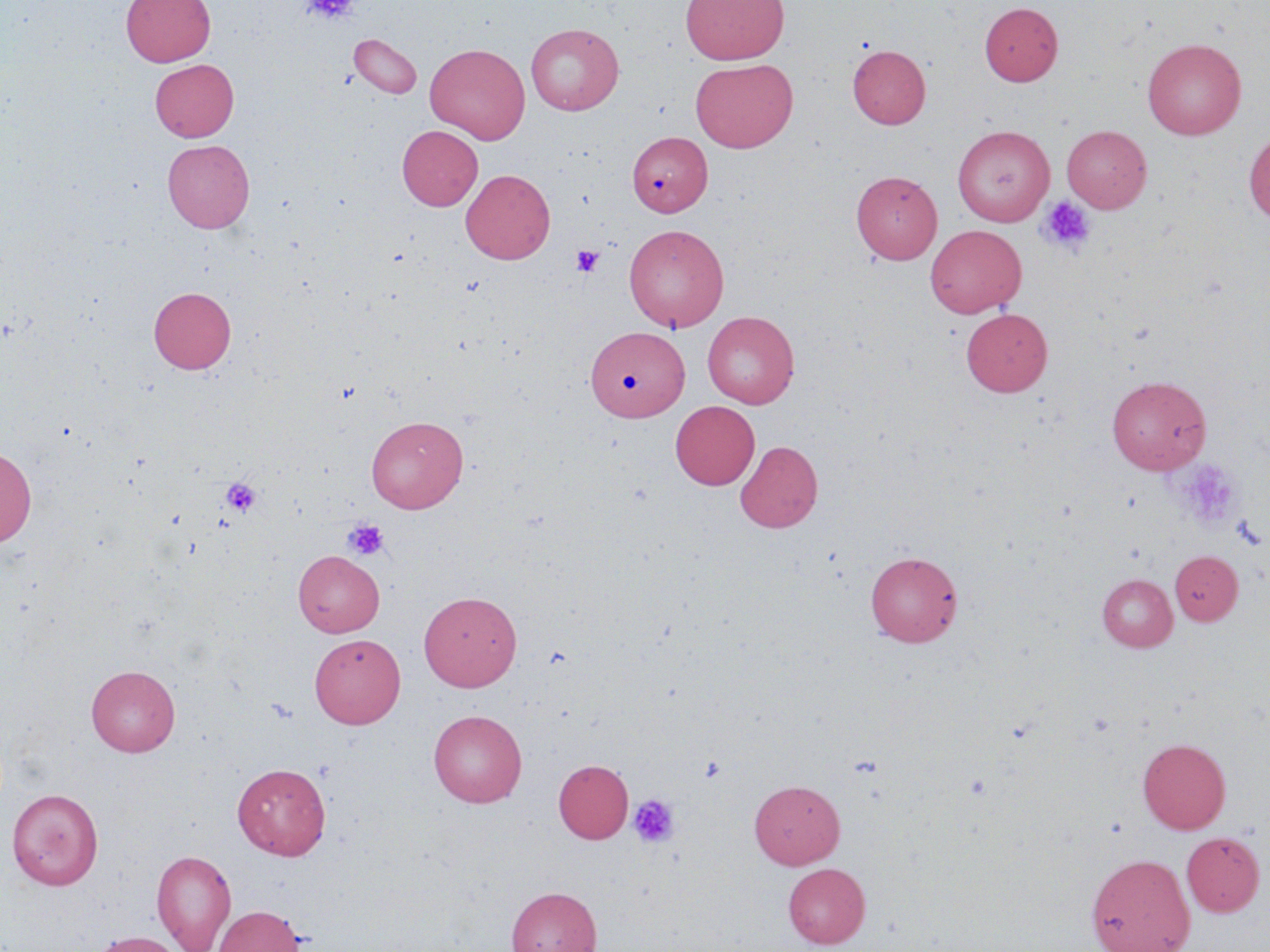
Summary:
  - Coordinate format: approximate bounding boxes as (x1, y1, x2, y2) in pixels
  - Platelet locations (subset): (302, 0, 360, 23), (1036, 195, 1096, 256), (571, 244, 604, 277), (1176, 459, 1242, 529), (221, 478, 261, 518), (342, 518, 389, 561), (699, 755, 726, 783), (628, 794, 680, 848)
  - Uninfected red blood cell locations (subset): (121, 0, 216, 66), (680, 0, 789, 64), (979, 2, 1062, 85), (525, 22, 624, 116), (349, 33, 422, 99), (1142, 38, 1246, 140), (425, 43, 530, 144), (848, 45, 931, 128), (150, 58, 239, 142), (690, 59, 798, 152), (397, 125, 482, 211), (953, 125, 1055, 226), (1244, 130, 1270, 224), (627, 132, 712, 217), (163, 139, 254, 233), (460, 169, 555, 264), (851, 170, 942, 264), (624, 223, 729, 332), (926, 225, 1026, 317), (148, 286, 236, 374), (961, 307, 1053, 396), (702, 311, 800, 409), (585, 326, 688, 422), (1107, 375, 1212, 474), (670, 401, 759, 489), (366, 415, 468, 513), (735, 440, 823, 533), (0, 446, 36, 549), (293, 550, 384, 637), (866, 551, 963, 647), (1169, 551, 1243, 625), (1097, 574, 1177, 651), (419, 590, 522, 690), (309, 633, 404, 728), (86, 664, 180, 756), (428, 709, 527, 807), (1137, 738, 1231, 834), (553, 759, 633, 843), (233, 763, 331, 860), (749, 779, 845, 869), (7, 789, 103, 890), (1181, 831, 1266, 916), (151, 849, 237, 951), (1086, 854, 1196, 952), (783, 863, 870, 948), (506, 886, 602, 952), (212, 905, 306, 952), (88, 931, 187, 952)
  - Slide-level diagnosis: no evidence of blood parasites
  - Magnification: 1000x
  - Modality: light microscopy
  - Image size: 1270×952 pixels
  - Field of view: one of a larger specimen
  - Stain: May-Grünwald-Giemsa
  - Preparation: thin blood smear